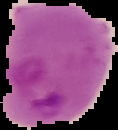

From a thin blood smear. Cell region segmented out of the field of view; the surrounding area is masked to black. Image is 118×130 pixels. Malaria status: parasitized.